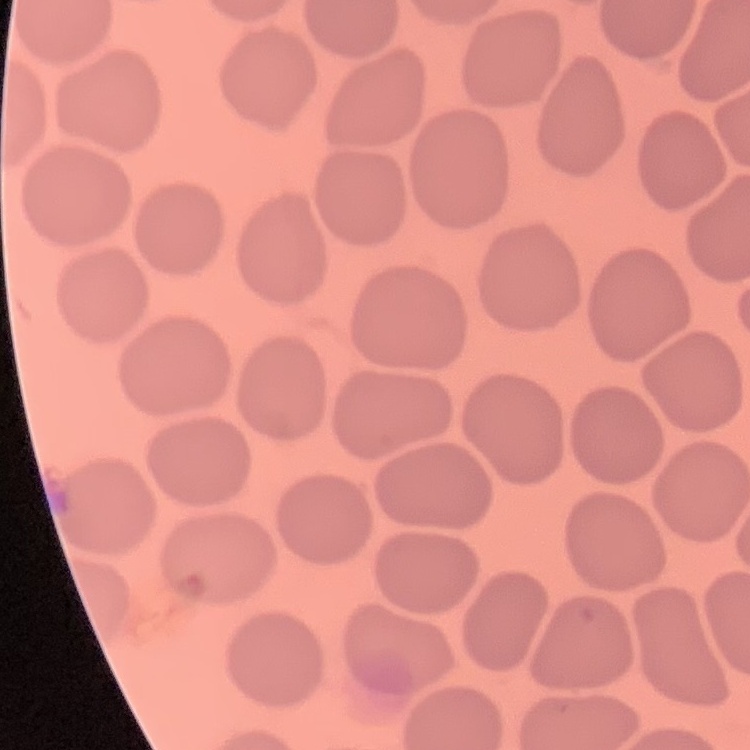
The red blood cells show no rouleaux formation. Thin blood film. Square crop of a larger photomicrograph. Stained with either Field's or Giemsa.